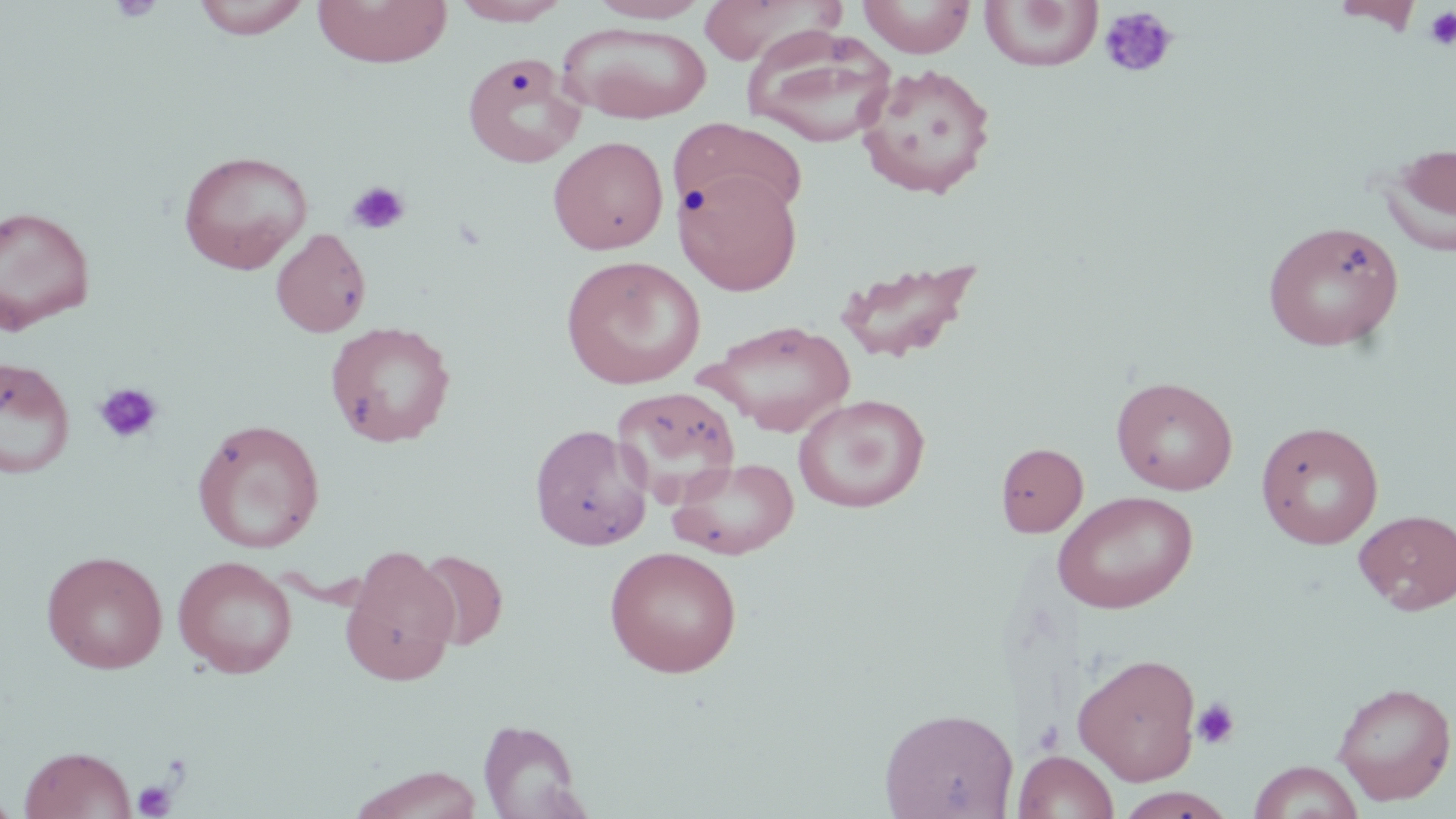
slide-level diagnosis = negative for blood parasites
image size = 1456×819 pixels
stain = May-Grünwald-Giemsa
uninfected red blood cell locations = approximate bounding boxes as named x1/y1/x2/y2 corners in pixels: (x1=191, y1=0, x2=313, y2=39), (x1=312, y1=0, x2=452, y2=68), (x1=451, y1=0, x2=572, y2=25), (x1=588, y1=0, x2=710, y2=23), (x1=858, y1=0, x2=976, y2=58), (x1=697, y1=1, x2=841, y2=65), (x1=980, y1=1, x2=1102, y2=72), (x1=1332, y1=1, x2=1424, y2=33), (x1=558, y1=23, x2=713, y2=123), (x1=743, y1=27, x2=897, y2=147), (x1=461, y1=53, x2=586, y2=168), (x1=856, y1=62, x2=997, y2=200), (x1=671, y1=118, x2=807, y2=226), (x1=548, y1=136, x2=669, y2=255), (x1=1379, y1=141, x2=1456, y2=259), (x1=178, y1=149, x2=314, y2=273), (x1=675, y1=170, x2=803, y2=296), (x1=0, y1=205, x2=96, y2=332), (x1=1262, y1=220, x2=1405, y2=352), (x1=269, y1=227, x2=372, y2=338), (x1=560, y1=255, x2=706, y2=390), (x1=833, y1=257, x2=983, y2=364), (x1=704, y1=319, x2=856, y2=436), (x1=325, y1=321, x2=456, y2=447), (x1=0, y1=355, x2=76, y2=479), (x1=1111, y1=375, x2=1238, y2=495), (x1=612, y1=386, x2=741, y2=505), (x1=793, y1=394, x2=930, y2=513), (x1=192, y1=418, x2=325, y2=553), (x1=1255, y1=421, x2=1384, y2=549), (x1=530, y1=423, x2=653, y2=551), (x1=995, y1=442, x2=1088, y2=537), (x1=668, y1=457, x2=800, y2=560), (x1=1052, y1=491, x2=1198, y2=614), (x1=1353, y1=508, x2=1456, y2=616), (x1=340, y1=545, x2=460, y2=685), (x1=604, y1=546, x2=743, y2=677), (x1=412, y1=549, x2=508, y2=649), (x1=41, y1=550, x2=168, y2=673), (x1=173, y1=555, x2=297, y2=678), (x1=1072, y1=652, x2=1202, y2=785), (x1=1332, y1=681, x2=1455, y2=805), (x1=879, y1=706, x2=1019, y2=819), (x1=478, y1=719, x2=587, y2=818), (x1=19, y1=745, x2=136, y2=819), (x1=1013, y1=750, x2=1119, y2=819), (x1=1248, y1=761, x2=1364, y2=819), (x1=348, y1=765, x2=484, y2=819), (x1=1115, y1=788, x2=1236, y2=819), (x1=0, y1=790, x2=19, y2=818)
platelet locations = approximate bounding boxes as named x1/y1/x2/y2 corners in pixels: (x1=108, y1=0, x2=164, y2=22), (x1=1098, y1=5, x2=1179, y2=80), (x1=1423, y1=6, x2=1456, y2=51), (x1=346, y1=180, x2=411, y2=236), (x1=94, y1=382, x2=163, y2=445), (x1=1192, y1=698, x2=1240, y2=749), (x1=1033, y1=720, x2=1065, y2=755), (x1=161, y1=751, x2=192, y2=784), (x1=133, y1=781, x2=176, y2=818)
magnification = 1000x
field of view = single
modality = optical microscopy
preparation = thin blood smear